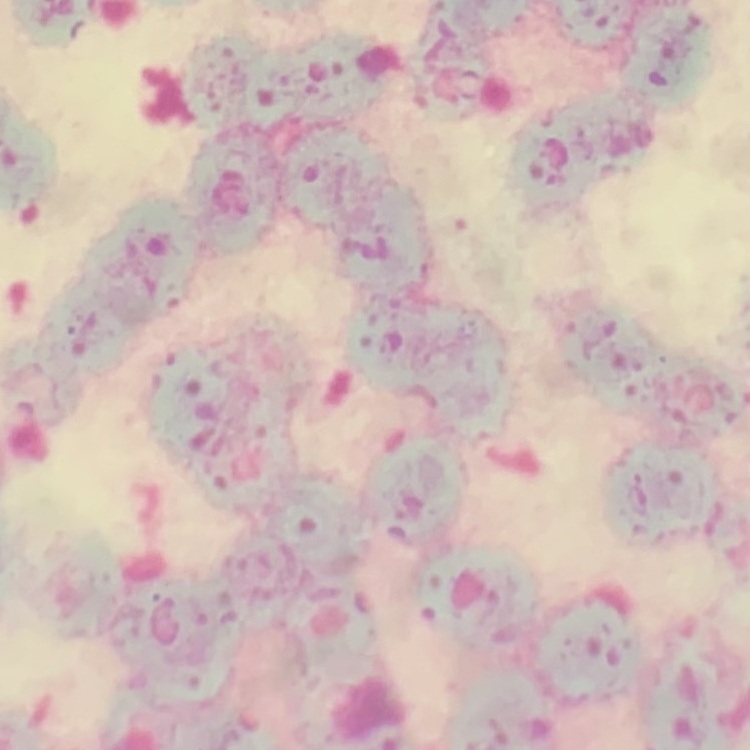

The red blood cells exhibit rouleaux formation. Stained with either Field's or Giemsa. One tile cut from a larger photomicrograph. Thin peripheral smear.